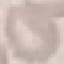 Result: no malaria parasites seen. Giemsa-stained preparation. Automatically extracted cell patch, resized to 64 × 64 pixels. Photographed with a smartphone camera at the microscope eyepiece. Thin blood smear.